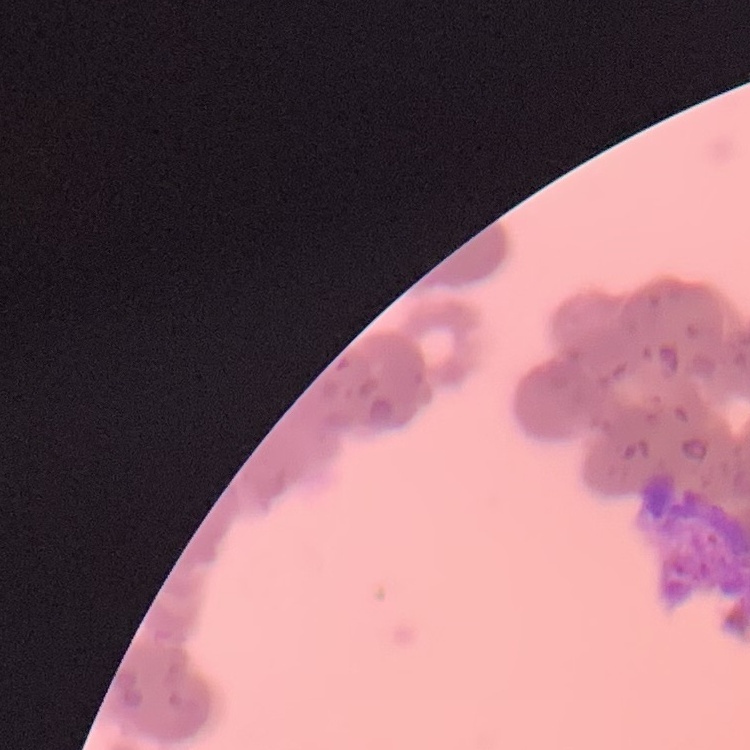

Summary:
  - Erythrocyte morphology: rouleaux formation
  - Preparation: thin peripheral smear
  - Image type: one tile cut from a larger photomicrograph
  - Stain: Field's or Giemsa